Assess the morphology of the erythrocytes.
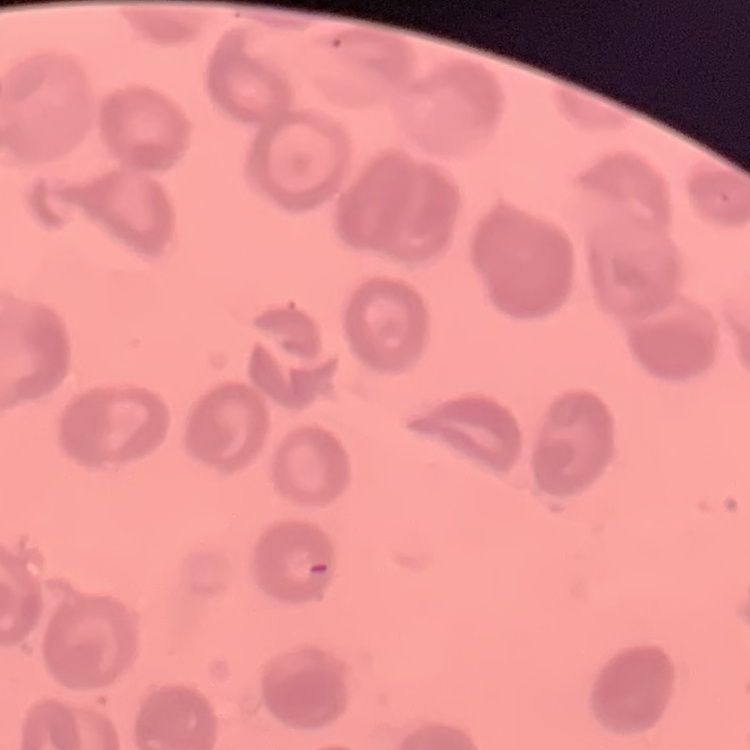
No rouleaux formation.

Thin blood smear. Square crop of a larger photomicrograph. Stained with either Field's or Giemsa.